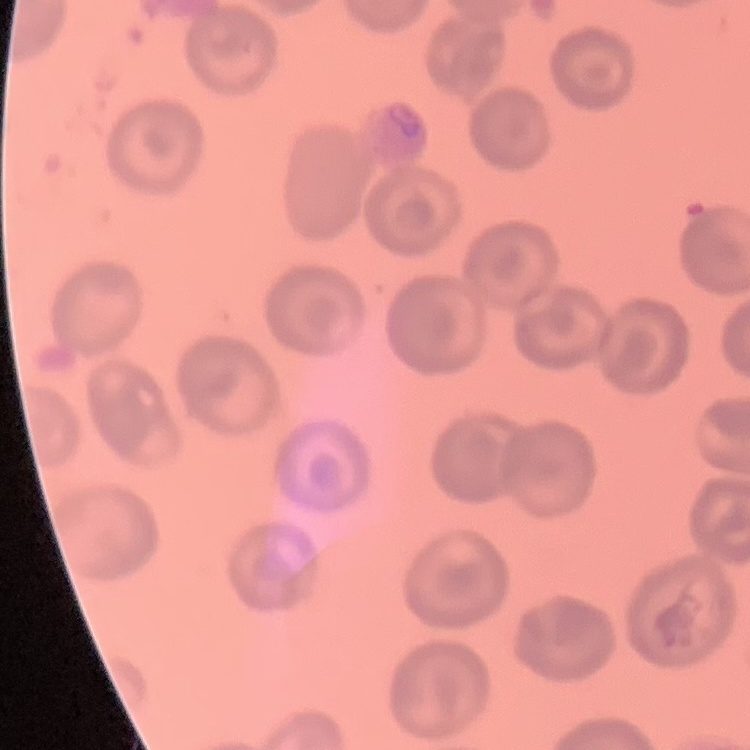

Summary:
  - Red blood cell morphology: no rouleaux formation
  - Preparation: thin blood smear
  - Image type: square crop of a larger photomicrograph
  - Stain: Field's or Giemsa